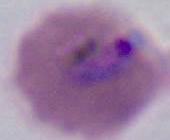
modality = photomicrograph
identification = Plasmodium
magnification = 400x or 1000x